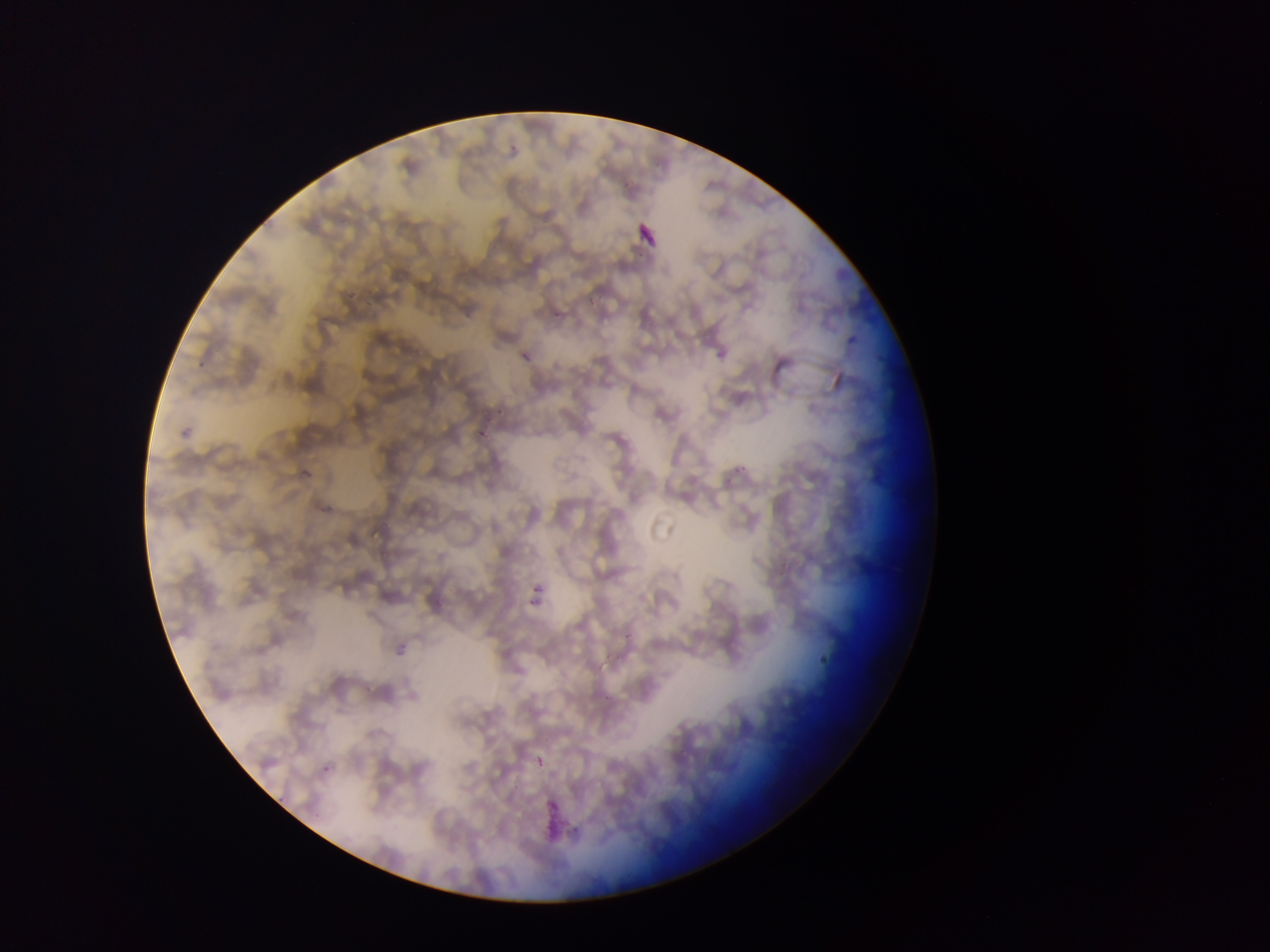 Approximate bounding boxes as {left, top, right, bottom} in pixels. Malaria parasite locations: {546, 313, 576, 323}, {842, 334, 861, 351}, {513, 340, 544, 364}, {193, 349, 216, 371}, {471, 418, 492, 446}, {180, 424, 201, 441}, {732, 464, 746, 474}, {290, 467, 316, 481}, {531, 583, 555, 597}, {521, 594, 538, 611}, {814, 643, 833, 665}, {533, 751, 550, 771}, {320, 763, 338, 780}, {275, 789, 291, 805}. Photographed through a microscope with a mobile-phone camera. Sample from Ghana. One field of view. Thin blood smear. Image is 1270×952 pixels.